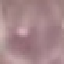

{
  "malaria_status": "uninfected",
  "image_type": "automatically extracted cell patch, resized to 64 × 64 pixels",
  "capture": "smartphone through the microscope eyepiece",
  "preparation": "thin blood smear",
  "stain": "Giemsa"
}